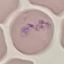

Malaria status: parasitized. Automatically extracted cell patch, resized to 64 × 64 pixels. Giemsa-stained preparation. Thin smear of blood. Photographed with a smartphone camera at the microscope eyepiece.